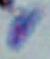
{
  "modality": "micrograph",
  "magnification": "1000x",
  "identification": "Toxoplasma gondii"
}